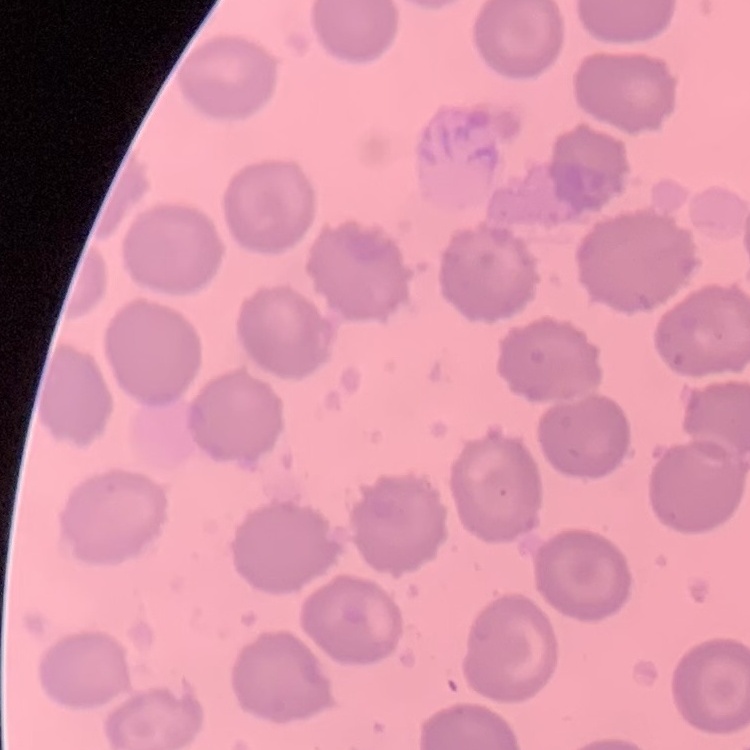

Summary:
  - Erythrocyte morphology: no rouleaux formation
  - Stain: Field's or Giemsa
  - Preparation: thin blood smear
  - Image type: square crop of a larger photomicrograph